Outline each blood parasite and name the species.
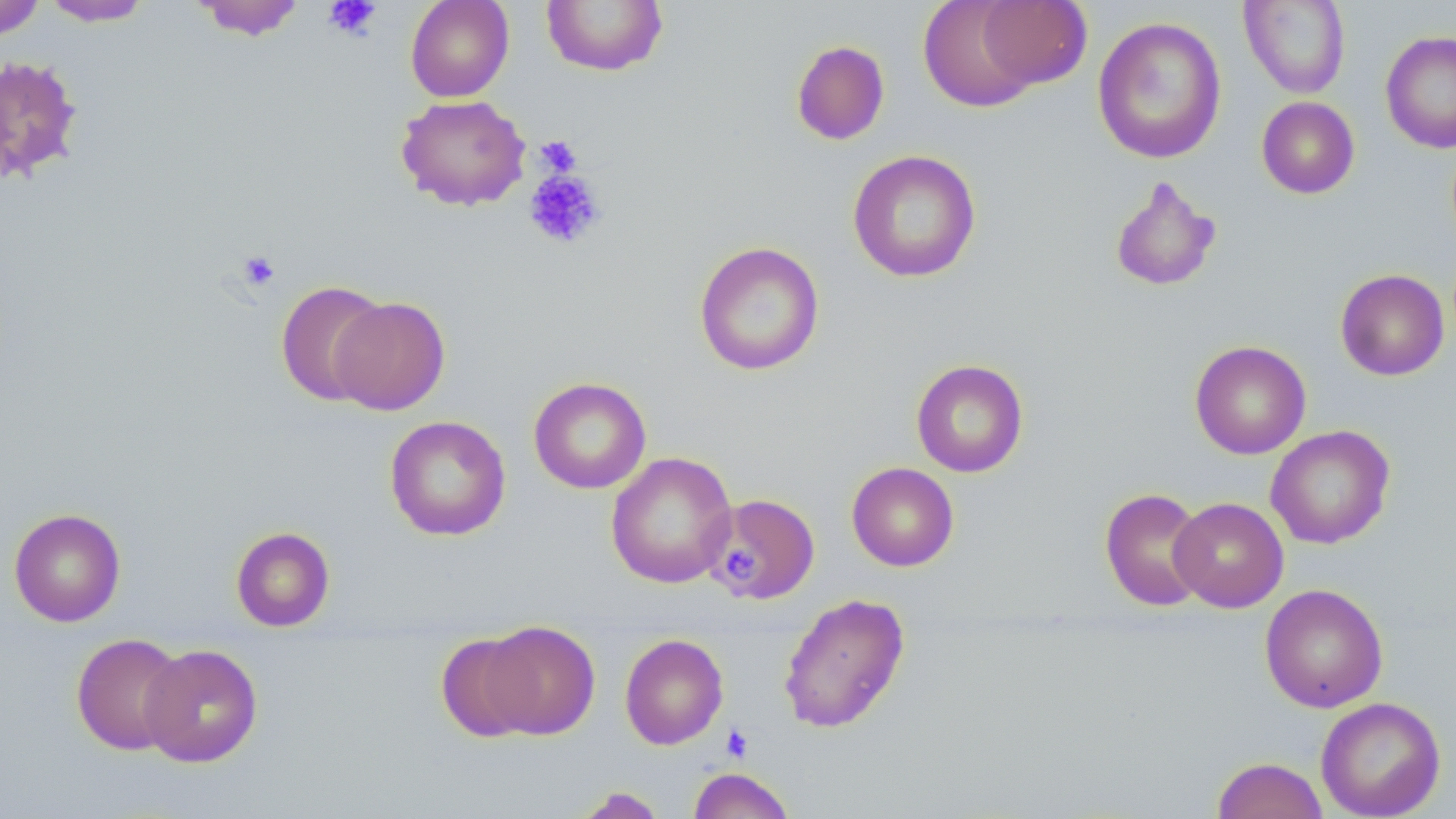
No blood parasites seen.

slide-level diagnosis = negative for blood parasites
image size = 1456×819 pixels
field of view = one of a larger specimen
preparation = thin blood film
magnification = 1000x
platelet locations = approximate bounding boxes as named x1/y1/x2/y2 corners in pixels: (x1=323, y1=0, x2=382, y2=40), (x1=535, y1=135, x2=582, y2=178), (x1=523, y1=169, x2=607, y2=249), (x1=237, y1=249, x2=280, y2=291), (x1=722, y1=548, x2=760, y2=580), (x1=721, y1=724, x2=753, y2=762)
stain = May-Grünwald-Giemsa
uninfected red blood cell locations = approximate bounding boxes as named x1/y1/x2/y2 corners in pixels: (x1=41, y1=0, x2=153, y2=26), (x1=191, y1=0, x2=308, y2=40), (x1=405, y1=0, x2=514, y2=102), (x1=917, y1=0, x2=1043, y2=112), (x1=975, y1=0, x2=1092, y2=91), (x1=0, y1=1, x2=45, y2=41), (x1=540, y1=1, x2=668, y2=76), (x1=1239, y1=1, x2=1351, y2=99), (x1=1092, y1=16, x2=1228, y2=164), (x1=1380, y1=30, x2=1456, y2=154), (x1=790, y1=40, x2=890, y2=145), (x1=0, y1=55, x2=85, y2=186), (x1=395, y1=94, x2=531, y2=211), (x1=1256, y1=96, x2=1360, y2=199), (x1=847, y1=150, x2=982, y2=283), (x1=1108, y1=175, x2=1222, y2=293), (x1=694, y1=241, x2=825, y2=376), (x1=1335, y1=269, x2=1449, y2=381), (x1=274, y1=280, x2=391, y2=406), (x1=330, y1=295, x2=451, y2=416), (x1=1189, y1=339, x2=1311, y2=459), (x1=911, y1=358, x2=1029, y2=478), (x1=528, y1=376, x2=652, y2=494), (x1=384, y1=415, x2=511, y2=541), (x1=1266, y1=425, x2=1395, y2=549), (x1=605, y1=452, x2=738, y2=589), (x1=846, y1=462, x2=959, y2=571), (x1=1099, y1=487, x2=1211, y2=612), (x1=706, y1=493, x2=819, y2=604), (x1=1168, y1=497, x2=1289, y2=612), (x1=8, y1=507, x2=126, y2=626), (x1=231, y1=526, x2=335, y2=631), (x1=1260, y1=583, x2=1388, y2=713), (x1=778, y1=592, x2=910, y2=734), (x1=479, y1=620, x2=601, y2=739), (x1=70, y1=632, x2=188, y2=755), (x1=436, y1=633, x2=541, y2=743), (x1=619, y1=633, x2=728, y2=750), (x1=138, y1=643, x2=263, y2=767), (x1=1315, y1=697, x2=1446, y2=819), (x1=1212, y1=756, x2=1329, y2=819), (x1=687, y1=767, x2=796, y2=819), (x1=571, y1=787, x2=668, y2=818)
modality = optical microscopy